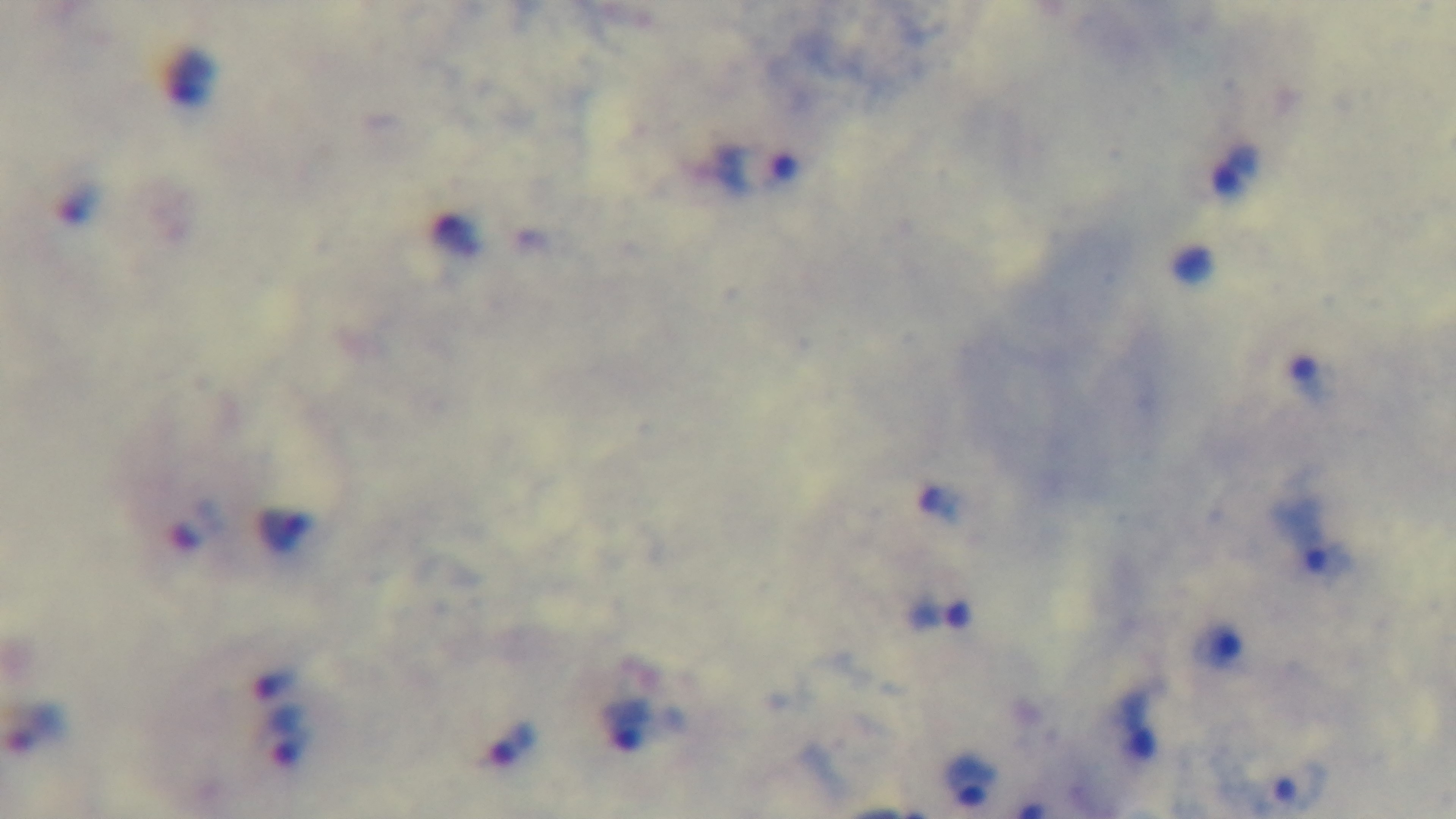
Photomicrograph. Preparation: thick blood film. Malaria status: infected. Single field of view. Captured with a mounted 4K digital camera. Oil-immersion objective, 100x. Giemsa stain.